Locate every uninfected red blood cell.
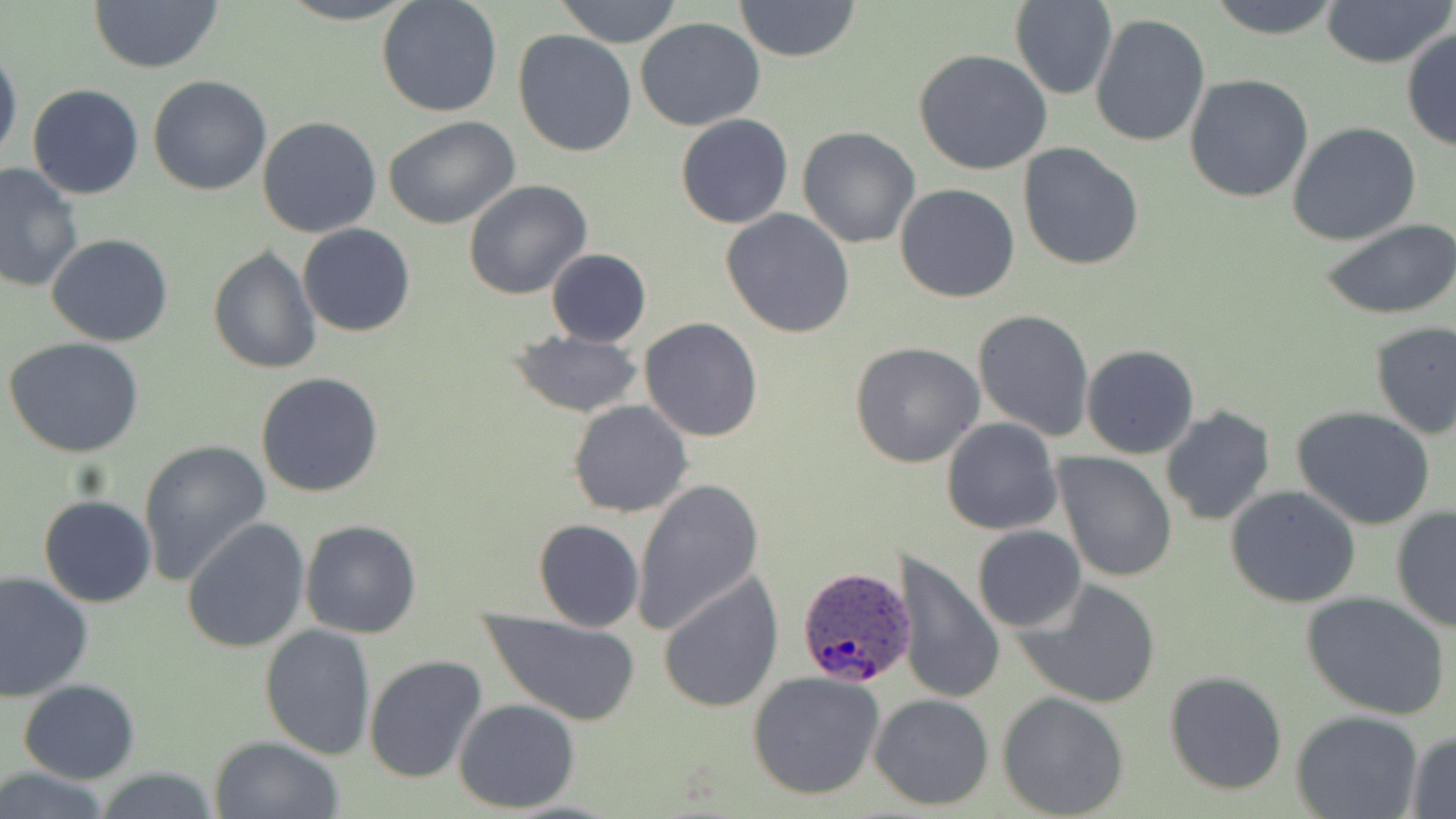
Approximate bounding boxes as (x1,y1)-(x2,y2) corner pairs in pixels.
Uninfected red blood cells: (271,0)-(423,24), (376,0)-(504,119), (552,0)-(684,46), (733,0)-(860,61), (1011,0)-(1118,100), (1204,0)-(1346,38), (88,1)-(222,74), (1319,1)-(1453,68), (1090,13)-(1210,148), (635,16)-(765,131), (1402,29)-(1456,155), (513,30)-(637,157), (0,40)-(22,168), (913,48)-(1056,176), (149,75)-(272,194), (1185,75)-(1314,204), (27,84)-(145,199), (675,113)-(793,228), (383,115)-(520,230), (258,117)-(383,238), (1288,122)-(1421,244), (798,126)-(922,248), (1017,143)-(1145,269), (0,162)-(84,297), (465,179)-(593,299), (895,183)-(1020,302), (722,208)-(855,338), (1321,219)-(1456,320), (298,223)-(416,337), (47,234)-(174,347), (207,245)-(320,375), (545,249)-(652,346), (971,309)-(1096,441), (638,318)-(763,442), (1369,321)-(1456,439), (507,329)-(645,418), (4,337)-(147,458), (850,341)-(984,467), (1081,345)-(1200,459), (255,372)-(386,498), (1071,372)-(1192,562), (568,400)-(694,517), (1161,406)-(1277,526), (1292,406)-(1437,530), (941,418)-(1064,536), (137,439)-(271,586), (1052,451)-(1177,583), (631,478)-(763,634), (1225,485)-(1362,608), (39,494)-(156,607), (1390,505)-(1456,634), (182,518)-(311,653), (300,519)-(422,639), (533,519)-(643,632), (973,526)-(1086,632), (899,551)-(1004,706), (657,570)-(783,714), (0,571)-(93,701), (1015,578)-(1163,710), (1301,592)-(1451,721), (480,610)-(642,724), (259,623)-(377,759), (364,655)-(489,785), (1164,670)-(1287,794), (746,671)-(886,799), (18,680)-(141,783), (997,692)-(1130,818), (869,693)-(995,811), (453,698)-(581,813), (1292,708)-(1422,818), (1404,730)-(1456,816), (209,735)-(343,819), (91,765)-(222,819), (0,766)-(112,819).

Summary:
  - Plasmodium ovale-infected red blood cell locations: (798,565)-(919,689)
  - Slide-level diagnosis: Plasmodium ovale
  - Field of view: single
  - Preparation: thin blood smear
  - Modality: light microscopy
  - Stain: May-Grünwald-Giemsa
  - Image size: 1456×819 pixels
  - Magnification: 1000x